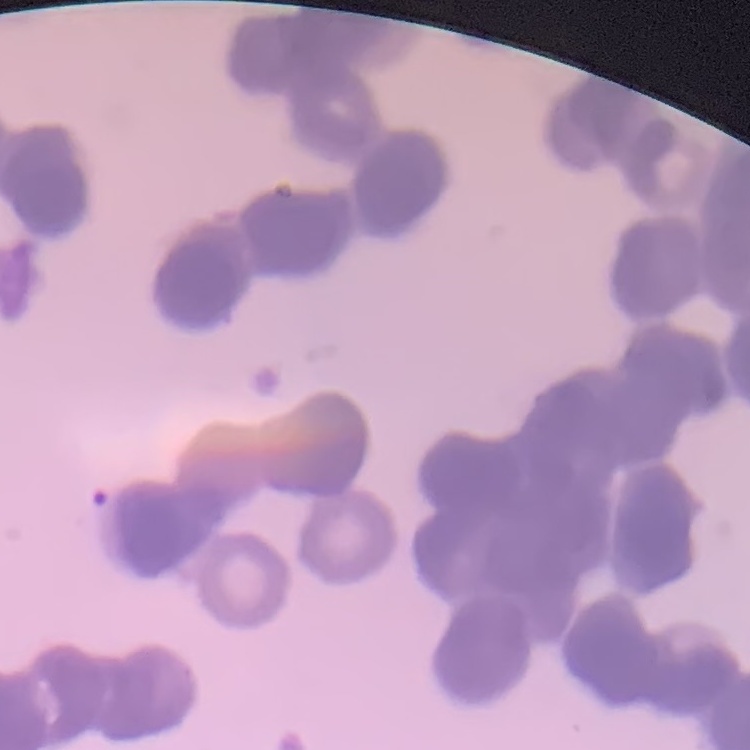
Summary:
  - Erythrocyte morphology: rouleaux formation
  - Stain: Field's or Giemsa
  - Image type: square crop of a larger photomicrograph
  - Preparation: thin blood smear